Locate every blood parasite and identify its species.
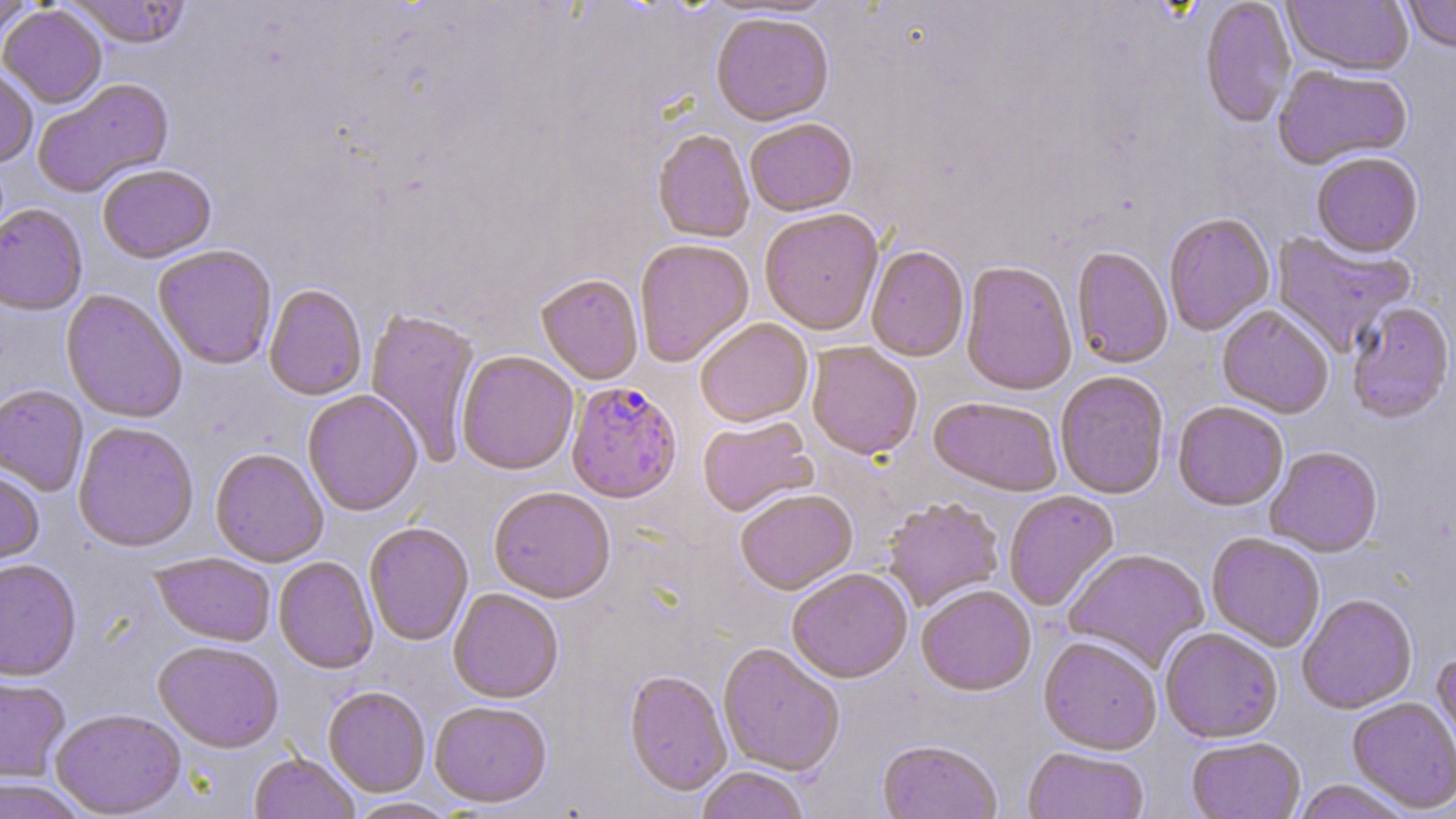
Approximate bounding boxes as [x1, y1, x2, y2] in pixels.
Plasmodium falciparum-infected red blood cells: [566, 382, 683, 504].
No Plasmodium ovale, Plasmodium malariae, Plasmodium vivax, Babesia divergens, or Trypanosoma brucei observed.

Uninfected red blood cell locations: [0, 0, 36, 37], [65, 0, 192, 50], [700, 0, 841, 21], [1200, 0, 1295, 131], [1282, 0, 1413, 80], [1402, 0, 1456, 56], [0, 6, 107, 110], [711, 16, 834, 129], [0, 65, 38, 168], [1273, 66, 1412, 172], [32, 79, 175, 198], [746, 121, 858, 219], [652, 132, 754, 245], [1311, 154, 1424, 261], [98, 166, 217, 265], [0, 205, 87, 317], [759, 211, 884, 337], [1164, 215, 1275, 336], [1271, 230, 1416, 358], [634, 241, 755, 369], [153, 246, 277, 370], [866, 248, 969, 363], [1070, 248, 1173, 370], [960, 263, 1077, 397], [536, 276, 643, 385], [264, 286, 366, 402], [61, 290, 187, 424], [1346, 304, 1454, 425], [1217, 307, 1333, 420], [365, 309, 480, 466], [695, 319, 813, 430], [807, 344, 922, 462], [457, 352, 579, 477], [1055, 372, 1169, 501], [0, 386, 88, 497], [303, 391, 423, 517], [928, 398, 1063, 498], [1173, 403, 1288, 513], [698, 417, 818, 518], [73, 423, 199, 554], [1265, 448, 1383, 559], [210, 450, 327, 567], [0, 469, 44, 572], [488, 489, 616, 604], [736, 491, 858, 597], [1004, 491, 1120, 612], [883, 498, 1004, 613], [364, 525, 473, 646], [1206, 533, 1325, 652], [1063, 549, 1211, 673], [150, 554, 275, 647], [274, 557, 378, 675], [0, 560, 82, 683], [787, 569, 913, 685], [917, 587, 1036, 698], [448, 590, 563, 705], [1297, 596, 1418, 714], [1160, 629, 1283, 744], [1038, 638, 1161, 756], [152, 642, 283, 754], [718, 644, 844, 777], [1432, 652, 1456, 764], [624, 671, 732, 798], [0, 674, 70, 784], [323, 688, 430, 798], [1347, 696, 1456, 814], [430, 703, 552, 810], [50, 710, 187, 818], [1187, 738, 1305, 819], [877, 741, 1002, 819], [1023, 748, 1148, 819], [249, 753, 360, 819], [695, 768, 810, 819], [0, 778, 86, 819], [1291, 780, 1413, 819], [345, 797, 461, 819]. Slide-level diagnosis: Plasmodium falciparum. Single field of view. May-Grünwald-Giemsa-stained preparation. Thin blood smear. Light microscopy. Captured at 1000x magnification. Image is 1456×819 pixels.